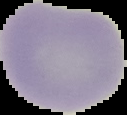 From a thin blood smear. Malaria status: uninfected. Cell region segmented out of the field of view; the surrounding area is masked to black. Image is 127×115 pixels.